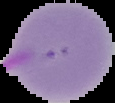

The area outside the segmented cell region is set to black. Result: malaria parasites identified. From a thin blood film. Image is 115×103 pixels.